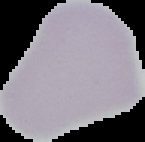

image_type: segmented cell region on a black background
image_size: 145×142 pixels
preparation: thin blood film
result: negative for Plasmodium parasites